Identify the parasite.
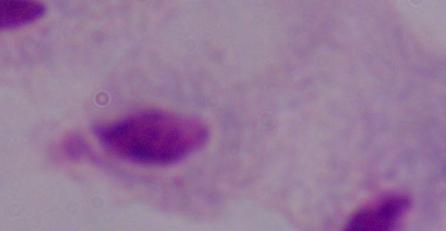

A trichomonad.

Captured at 1000x magnification. Photomicrograph.